Comment on the morphology of the red blood cells.
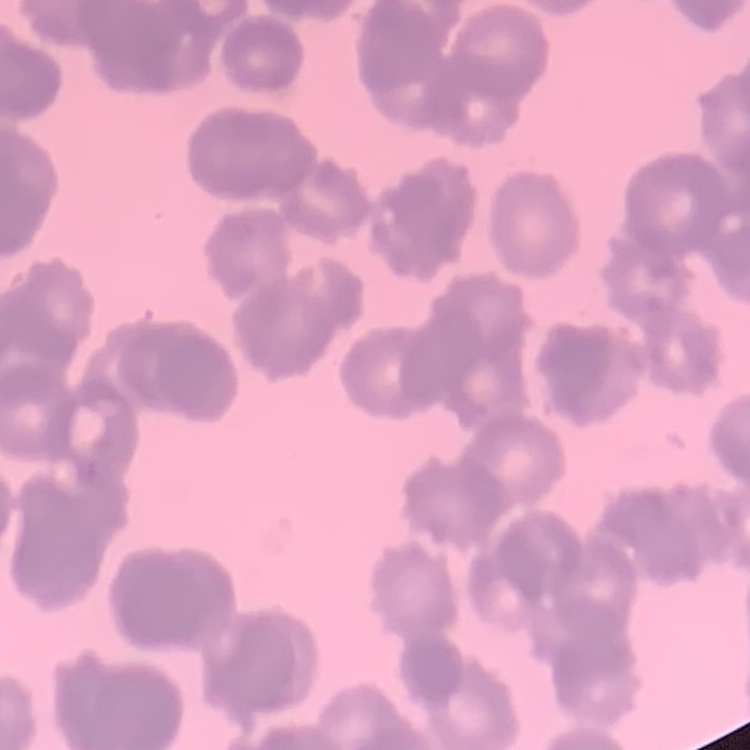
Rouleaux formation.

One tile cut from a larger photomicrograph. Field's or Giemsa stain. Thin blood film.